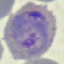
Result: malaria parasites detected. Giemsa-stained preparation. Acquired by smartphone through the microscope eyepiece. Automatically extracted cell patch, resized to 64 × 64 pixels. Thin blood film.